Assess the morphology of the erythrocytes.
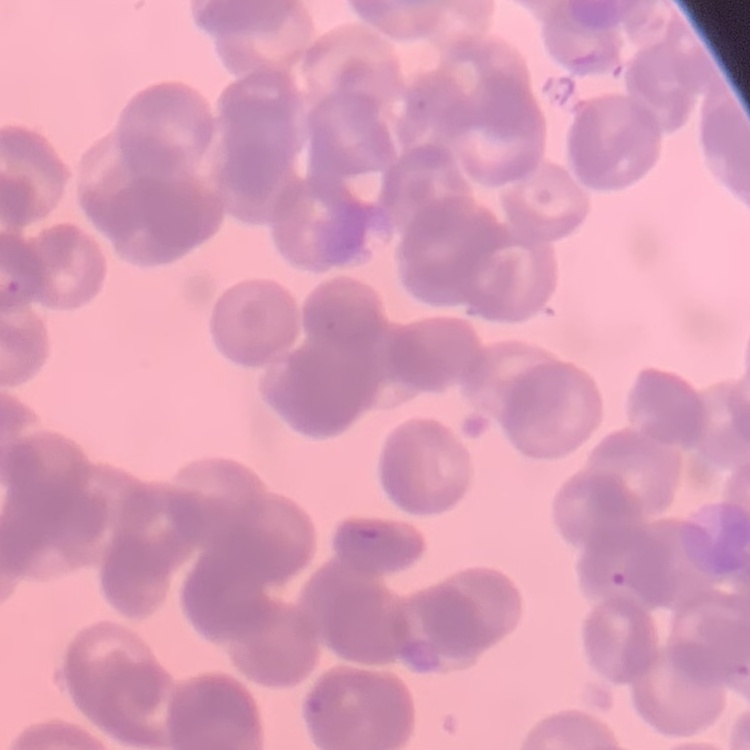

Rouleaux formation.

Summary:
  - Preparation: thin peripheral smear
  - Image type: one tile cut from a larger photomicrograph
  - Stain: Field's or Giemsa